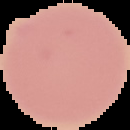
Summary:
  - Image size: 130×130 pixels
  - Preparation: thin blood smear
  - Image type: segmented cell region with the area outside set to black
  - Malaria status: uninfected